Assess this cell for malaria.
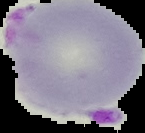

It is parasitized.

Summary:
  - Preparation: thin blood smear
  - Image type: segmented cell region on a black background
  - Image size: 145×133 pixels